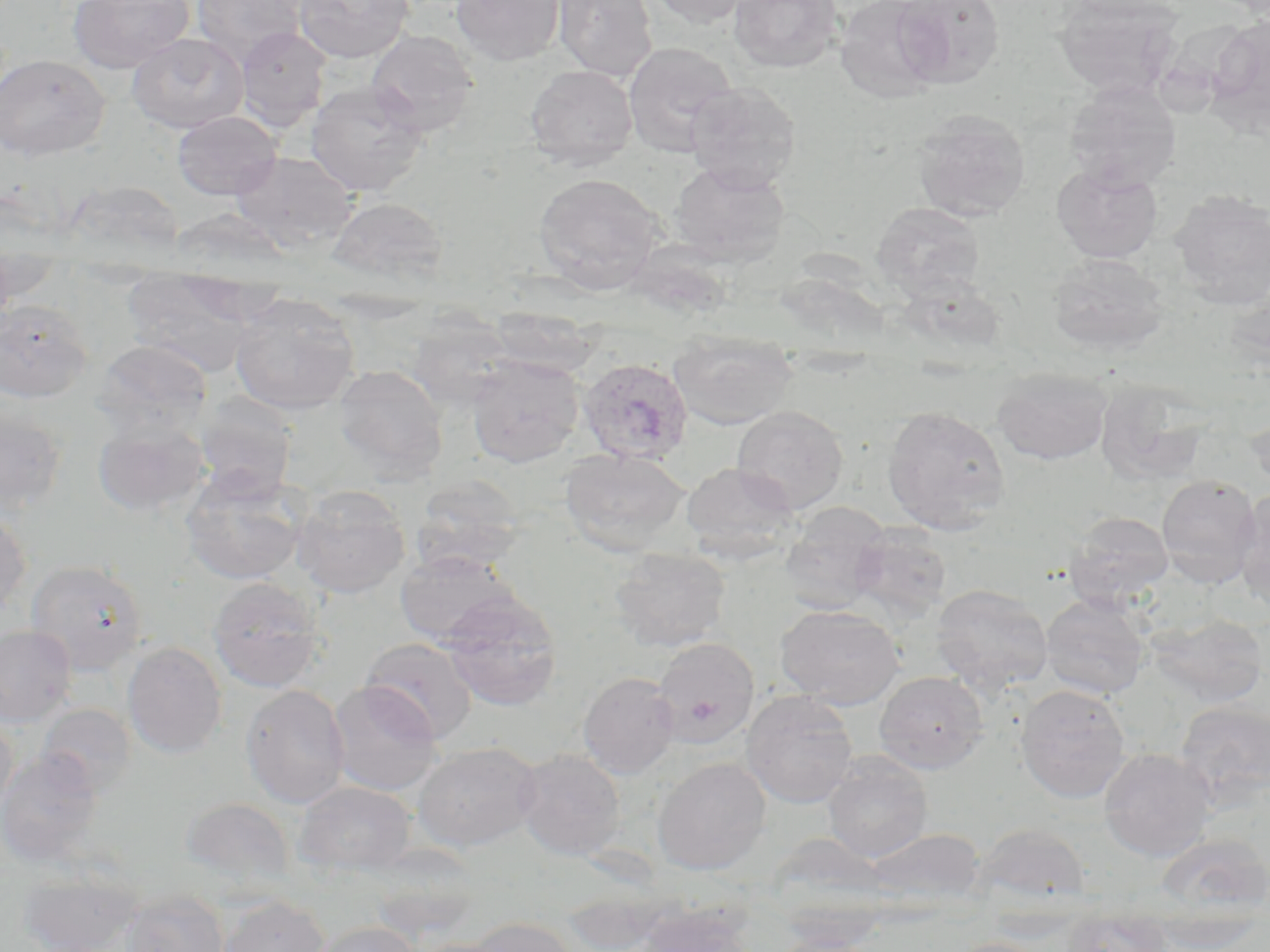
slide-level diagnosis = Plasmodium ovale
magnification = 1000x
field of view = single
preparation = thin blood smear
image size = 1270×952 pixels
modality = optical microscopy
uninfected red blood cell locations = approximate bounding boxes as (x1, y1, x2, y2) in pixels: (68, 0, 195, 73), (192, 0, 307, 65), (293, 0, 414, 63), (450, 0, 565, 66), (554, 0, 658, 81), (643, 0, 764, 27), (729, 0, 842, 74), (834, 0, 947, 102), (892, 0, 1005, 87), (1054, 0, 1184, 98), (1207, 15, 1270, 129), (235, 25, 332, 132), (366, 30, 479, 136), (128, 32, 249, 133), (622, 41, 738, 157), (0, 54, 109, 161), (525, 64, 638, 171), (305, 81, 429, 197), (1063, 81, 1182, 191), (684, 82, 802, 191), (172, 110, 282, 200), (912, 110, 1032, 222), (230, 151, 360, 252), (669, 160, 790, 264), (1052, 162, 1162, 263), (533, 172, 664, 291), (59, 180, 186, 259), (1168, 190, 1270, 310), (327, 196, 449, 285), (872, 202, 985, 299), (1046, 253, 1169, 356), (1, 258, 64, 304), (122, 274, 264, 375), (230, 294, 360, 416), (0, 299, 93, 403), (487, 306, 600, 376), (406, 313, 517, 412), (668, 330, 797, 430), (94, 339, 212, 436), (466, 354, 584, 467), (333, 364, 449, 481), (991, 368, 1113, 465), (1094, 379, 1212, 487), (193, 394, 298, 500), (0, 402, 68, 515), (882, 404, 1011, 534), (732, 406, 849, 514), (1245, 409, 1270, 493), (92, 417, 210, 517), (559, 448, 691, 556), (681, 462, 800, 563), (180, 470, 308, 586), (1156, 474, 1262, 587), (409, 477, 527, 576), (291, 486, 410, 599), (1234, 490, 1270, 610), (778, 501, 892, 613), (0, 506, 31, 619), (1064, 510, 1174, 606), (1058, 512, 1164, 698), (850, 524, 952, 624), (609, 547, 730, 652), (394, 549, 523, 646), (25, 558, 148, 676), (207, 577, 327, 693), (931, 583, 1054, 694), (440, 592, 563, 711), (1041, 594, 1151, 699), (775, 605, 904, 709), (1147, 612, 1268, 706), (0, 625, 77, 726), (360, 637, 478, 743), (652, 638, 759, 747), (122, 641, 227, 758), (874, 670, 988, 774), (578, 671, 680, 778), (327, 681, 443, 796), (1015, 684, 1130, 803), (241, 685, 350, 809), (741, 690, 858, 808), (1176, 700, 1270, 804), (37, 703, 137, 798), (0, 712, 19, 817), (412, 741, 542, 852), (1099, 747, 1216, 861), (0, 749, 104, 867), (513, 749, 627, 861), (823, 752, 933, 863), (652, 757, 771, 874), (293, 781, 417, 877), (180, 797, 295, 891), (975, 823, 1091, 906), (862, 827, 988, 909), (1155, 833, 1269, 917), (365, 850, 483, 942), (19, 870, 142, 952), (561, 886, 679, 951), (120, 889, 229, 952), (218, 895, 329, 952), (633, 901, 757, 952), (980, 912, 1093, 944), (462, 916, 581, 952), (1060, 920, 1173, 952), (309, 921, 420, 952), (1148, 921, 1263, 950), (771, 931, 884, 951), (950, 936, 1054, 952)
stain = May-Grünwald-Giemsa
Plasmodium ovale-infected red blood cell locations = approximate bounding boxes as (x1, y1, x2, y2) in pixels: (578, 357, 694, 465)